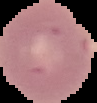
Summary:
  - Image size: 97×103 pixels
  - Image type: segmented cell region on a black background
  - Malaria status: uninfected
  - Preparation: thin blood smear